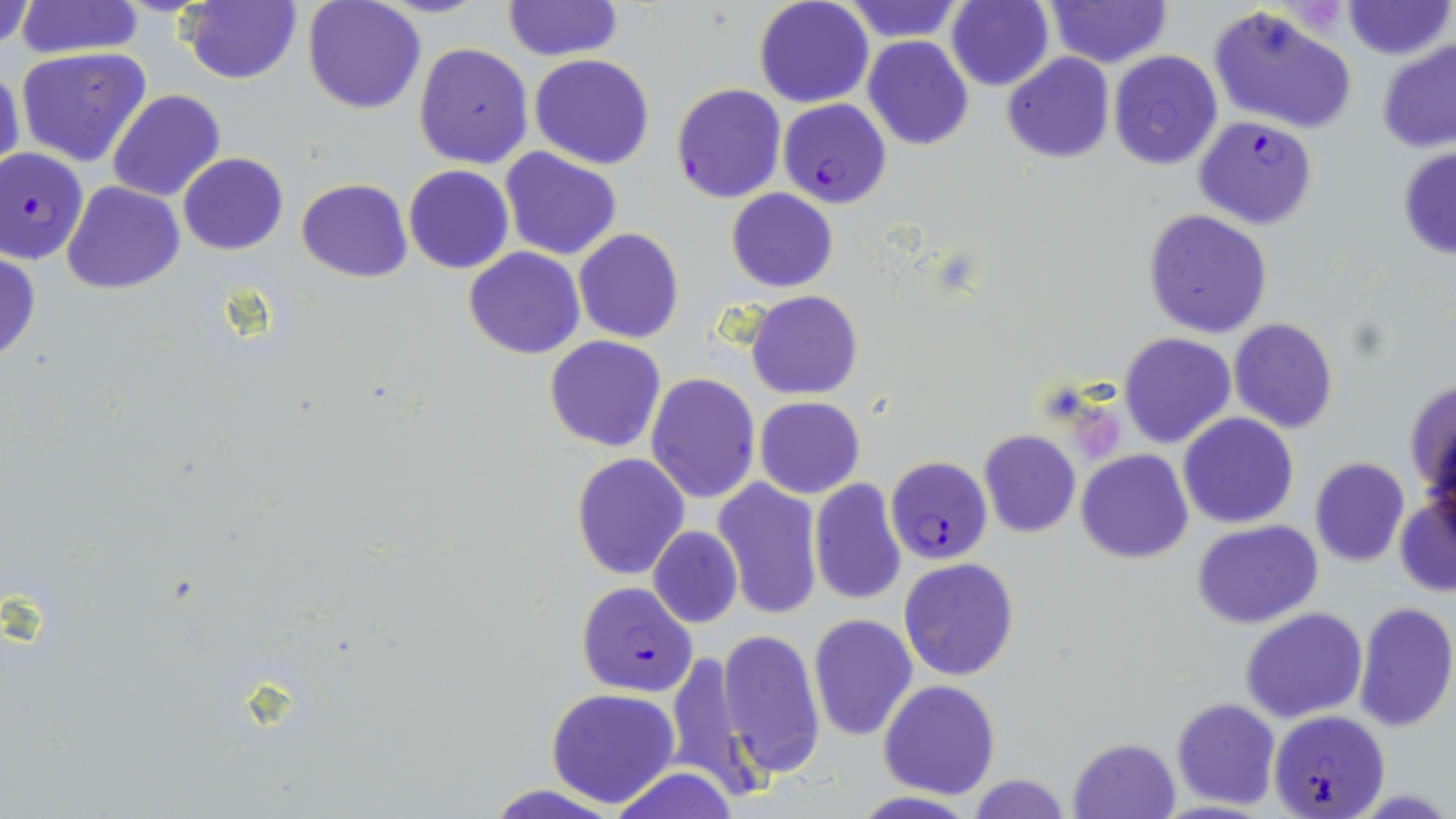

Summary:
  - Coordinate format: approximate bounding boxes as (x1,y1)-(x2,y2) corner pairs in pixels
  - Plasmodium falciparum-infected red blood cell locations: (670,83)-(786,204), (777,97)-(892,209), (1194,116)-(1317,230), (0,146)-(90,265), (885,455)-(993,566), (575,581)-(699,695), (1269,707)-(1391,818)
  - Uninfected red blood cell locations: (183,0)-(300,85), (501,0)-(620,60), (753,0)-(874,108), (842,0)-(966,40), (1046,0)-(1168,67), (1343,0)-(1452,60), (0,1)-(35,52), (15,1)-(146,59), (302,1)-(426,114), (945,1)-(1055,90), (1208,4)-(1357,134), (862,36)-(973,150), (1377,36)-(1456,152), (413,41)-(534,169), (16,47)-(152,167), (1108,50)-(1223,171), (528,53)-(656,170), (1002,53)-(1114,163), (0,64)-(26,182), (107,89)-(227,202), (1397,145)-(1456,261), (499,147)-(623,260), (177,154)-(289,255), (403,165)-(514,275), (298,179)-(412,282), (61,180)-(184,294), (725,186)-(839,292), (1142,208)-(1273,338), (573,229)-(684,344), (463,247)-(585,359), (0,251)-(41,363), (746,291)-(861,400), (1227,318)-(1339,435), (1118,332)-(1235,448), (544,336)-(667,454), (645,373)-(760,503), (1404,376)-(1456,502), (754,397)-(865,498), (1178,412)-(1299,529), (977,430)-(1082,539), (1078,450)-(1192,563), (571,452)-(690,579), (1309,457)-(1410,567), (713,478)-(824,620), (808,478)-(908,607), (1394,496)-(1455,596), (1192,520)-(1323,629), (647,524)-(742,629), (899,557)-(1020,681), (1353,602)-(1456,732), (1239,608)-(1369,724), (808,614)-(917,741), (716,627)-(825,780), (665,648)-(765,803), (879,680)-(1001,800), (545,688)-(680,809), (1170,697)-(1281,809), (1069,737)-(1180,818), (607,766)-(742,819), (968,775)-(1073,818), (848,791)-(981,819)
  - Platelet locations: (1077,413)-(1123,463)
  - Slide-level diagnosis: Plasmodium falciparum
  - Field of view: single
  - Image size: 1456×819 pixels
  - Stain: May-Grünwald-Giemsa
  - Magnification: 1000x
  - Modality: optical microscopy
  - Preparation: thin blood film